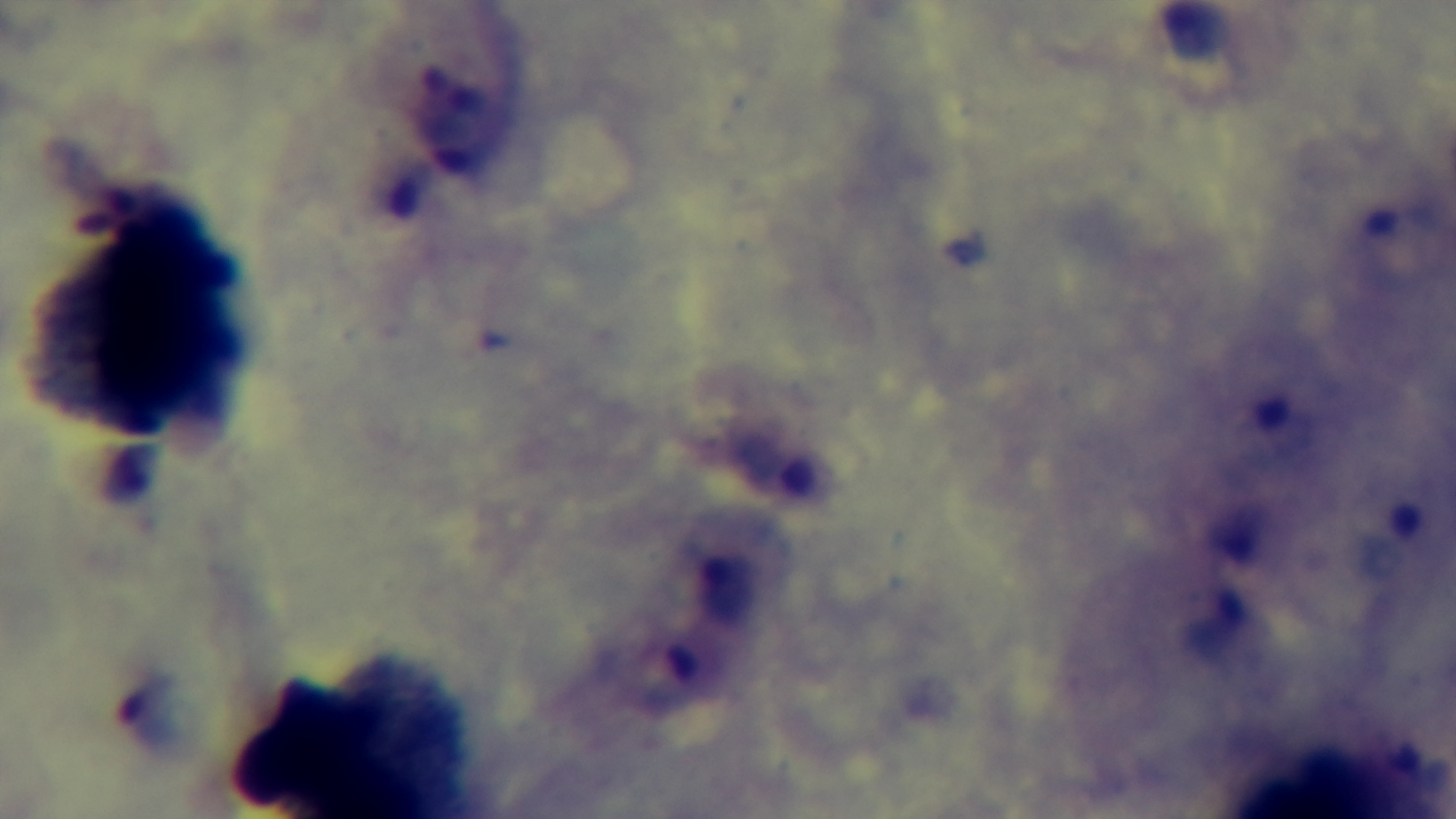
Giemsa-stained. 100x oil-immersion objective. Photomicrograph. Preparation: thick smear. Mounted 4K digital camera. Malaria status: positive. One field from the slide.